Name the parasite shown.
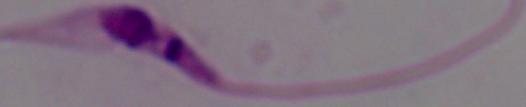
This is Leishmania.

modality: photomicrograph
magnification: 1000x